Locate every blood parasite and identify its species.
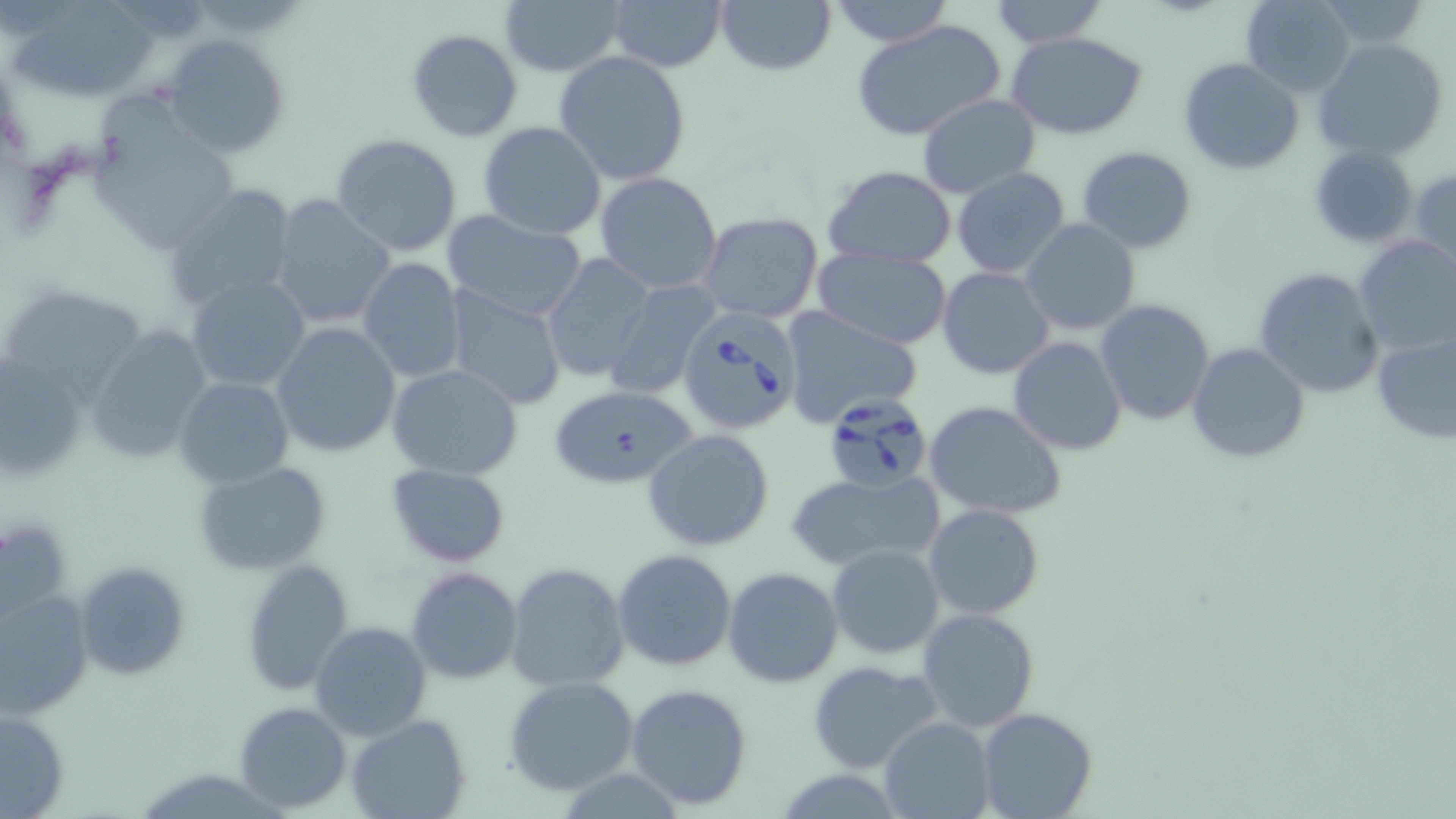
Approximate bounding boxes as named x1/y1/x2/y2 corners in pixels.
Babesia divergens-infected red blood cells: (x1=677, y1=311, x2=804, y2=436), (x1=821, y1=395, x2=934, y2=493).
No Plasmodium falciparum, Plasmodium ovale, Plasmodium malariae, Plasmodium vivax, or Trypanosoma brucei observed.

slide-level diagnosis = Babesia divergens
stain = May-Grünwald-Giemsa
image size = 1456×819 pixels
magnification = 1000x
field of view = one of a larger specimen
uninfected red blood cell locations = approximate bounding boxes as named x1/y1/x2/y2 corners in pixels: (x1=500, y1=0, x2=626, y2=76), (x1=609, y1=0, x2=726, y2=73), (x1=716, y1=0, x2=837, y2=77), (x1=828, y1=0, x2=954, y2=48), (x1=1239, y1=0, x2=1355, y2=96), (x1=987, y1=1, x2=1109, y2=47), (x1=11, y1=3, x2=156, y2=104), (x1=851, y1=18, x2=1008, y2=143), (x1=407, y1=28, x2=524, y2=144), (x1=1006, y1=31, x2=1149, y2=140), (x1=162, y1=32, x2=290, y2=159), (x1=1312, y1=39, x2=1449, y2=162), (x1=554, y1=51, x2=691, y2=186), (x1=1177, y1=56, x2=1306, y2=176), (x1=916, y1=93, x2=1040, y2=200), (x1=96, y1=96, x2=244, y2=256), (x1=477, y1=122, x2=607, y2=240), (x1=330, y1=134, x2=462, y2=258), (x1=1309, y1=144, x2=1421, y2=249), (x1=1077, y1=145, x2=1198, y2=254), (x1=824, y1=166, x2=956, y2=270), (x1=1409, y1=166, x2=1456, y2=278), (x1=951, y1=168, x2=1070, y2=279), (x1=594, y1=172, x2=724, y2=296), (x1=162, y1=183, x2=299, y2=313), (x1=267, y1=194, x2=397, y2=332), (x1=442, y1=210, x2=589, y2=324), (x1=696, y1=213, x2=823, y2=324), (x1=1020, y1=219, x2=1140, y2=337), (x1=1352, y1=235, x2=1456, y2=360), (x1=812, y1=247, x2=955, y2=348), (x1=965, y1=247, x2=1104, y2=369), (x1=541, y1=253, x2=658, y2=384), (x1=356, y1=258, x2=464, y2=385), (x1=937, y1=267, x2=1055, y2=380), (x1=1252, y1=267, x2=1386, y2=398), (x1=185, y1=274, x2=312, y2=394), (x1=600, y1=280, x2=719, y2=399), (x1=0, y1=285, x2=151, y2=405), (x1=444, y1=286, x2=568, y2=411), (x1=1094, y1=298, x2=1215, y2=427), (x1=780, y1=305, x2=924, y2=430), (x1=86, y1=323, x2=213, y2=463), (x1=270, y1=323, x2=402, y2=456), (x1=1371, y1=324, x2=1456, y2=446), (x1=1008, y1=336, x2=1127, y2=456), (x1=1186, y1=342, x2=1310, y2=462), (x1=1, y1=354, x2=89, y2=486), (x1=388, y1=363, x2=524, y2=481), (x1=174, y1=376, x2=293, y2=487), (x1=549, y1=384, x2=698, y2=489), (x1=924, y1=400, x2=1067, y2=521), (x1=645, y1=429, x2=776, y2=552), (x1=193, y1=461, x2=334, y2=575), (x1=386, y1=464, x2=511, y2=566), (x1=785, y1=470, x2=944, y2=571), (x1=922, y1=503, x2=1045, y2=621), (x1=1, y1=514, x2=74, y2=627), (x1=826, y1=543, x2=944, y2=660), (x1=612, y1=548, x2=738, y2=673), (x1=74, y1=561, x2=191, y2=682), (x1=240, y1=561, x2=354, y2=696), (x1=505, y1=563, x2=630, y2=692), (x1=406, y1=566, x2=524, y2=684), (x1=722, y1=567, x2=844, y2=688), (x1=0, y1=587, x2=95, y2=718), (x1=916, y1=606, x2=1039, y2=733), (x1=309, y1=620, x2=432, y2=739), (x1=807, y1=660, x2=944, y2=774), (x1=502, y1=676, x2=641, y2=796), (x1=624, y1=684, x2=753, y2=811), (x1=233, y1=701, x2=352, y2=814), (x1=0, y1=706, x2=71, y2=817), (x1=977, y1=708, x2=1099, y2=819), (x1=346, y1=712, x2=471, y2=819), (x1=878, y1=716, x2=995, y2=819)
modality = optical microscopy
preparation = thin blood smear